Classify this cell by malaria status.
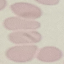

Uninfected.

Giemsa-stained preparation. Acquired by smartphone through the microscope eyepiece. Thin blood film. Cell patch, automatically extracted from a larger field of view and resized to 64 × 64 pixels.